Assess the morphology of the red blood cells.
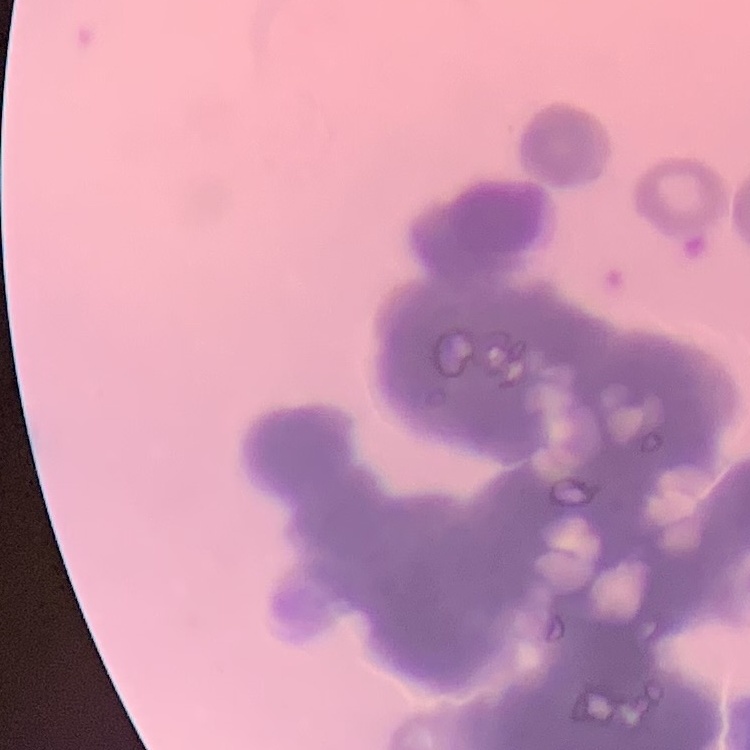
Rouleaux formation.

stain: Field's or Giemsa
preparation: thin peripheral smear
image_type: one tile cut from a larger photomicrograph